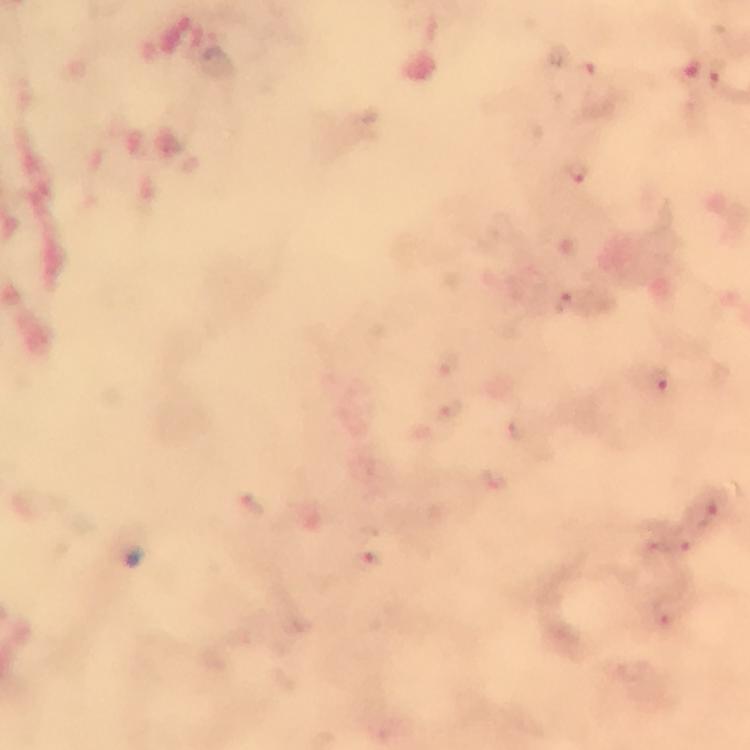 Approximate centers as [x, y] in pixels. Malaria parasite locations: [583, 72], [718, 72], [575, 170], [568, 301], [447, 362], [660, 380], [451, 409], [494, 477], [252, 503], [707, 505], [683, 541], [368, 556], [663, 612]. Thick blood film. Photographed through the microscope with a smartphone camera. Cropped region of a single field of view. Immersion oil was used. Giemsa stain. Image is 750×750 pixels. From a malaria diagnostic workup. 100x magnification.